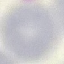
result = no malaria parasites seen
preparation = thin blood film
image type = cell patch, automatically extracted from a larger field of view and resized to 64 × 64 pixels
stain = Giemsa
capture = smartphone camera at the microscope eyepiece